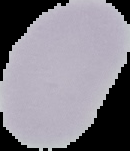
image size = 130×151 pixels
preparation = thin blood smear
image type = segmented cell region with the area outside set to black
result = no Plasmodium parasites detected